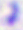

Photomicrograph. Captured at 400x magnification. Toxoplasma gondii is seen.